Locate every Plasmodium ovale-infected red blood cell.
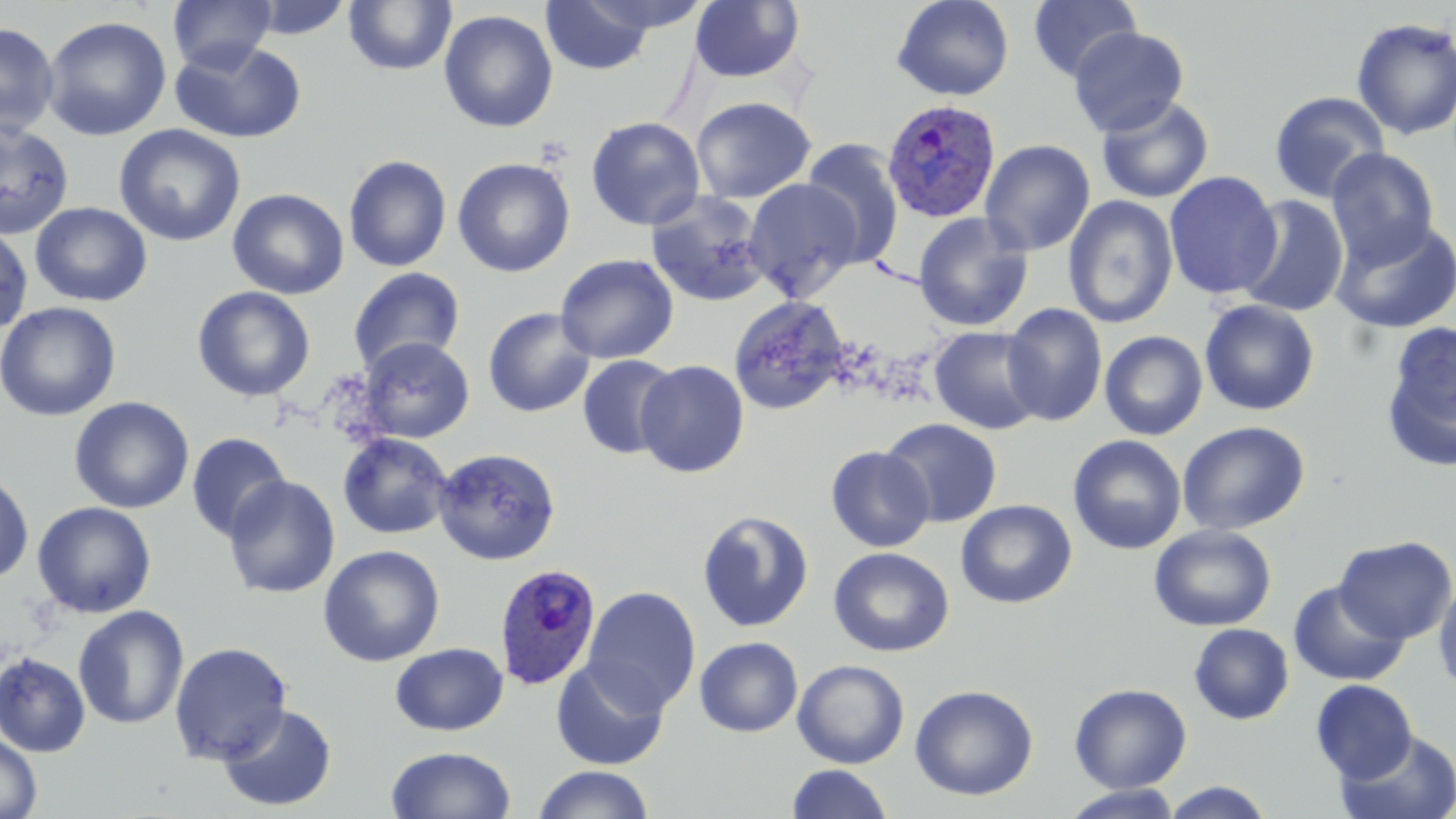

Approximate bounding boxes as (x1,y1)-(x2,y2) corner pairs in pixels.
Plasmodium ovale-infected red blood cells: (882,99)-(1001,223), (494,564)-(602,690).

{
  "slide_level_diagnosis": "Plasmodium ovale",
  "uninfected_red_blood_cell_locations": "approximate bounding boxes as (x1,y1)-(x2,y2) corner pairs in pixels: (168,0)-(276,73), (572,0)-(713,35), (891,0)-(1015,101), (1027,0)-(1142,83), (245,1)-(355,40), (343,1)-(457,75), (540,1)-(658,75), (690,1)-(805,83), (438,10)-(558,133), (42,15)-(172,141), (1350,17)-(1456,141), (0,23)-(59,137), (1069,26)-(1189,136), (170,38)-(306,145), (1269,91)-(1390,203), (690,96)-(816,203), (1095,96)-(1214,204), (586,116)-(705,230), (0,121)-(74,240), (114,124)-(246,247), (799,138)-(906,269), (979,139)-(1096,256), (1326,148)-(1439,266), (343,154)-(452,272), (452,157)-(575,278), (1164,171)-(1283,299), (743,178)-(864,301), (227,188)-(349,300), (646,190)-(769,307), (1236,195)-(1350,318), (1063,196)-(1178,328), (30,201)-(152,307), (913,212)-(1033,332), (1330,218)-(1456,335), (0,223)-(33,336), (555,253)-(679,364), (347,267)-(466,376), (192,286)-(315,401), (728,295)-(850,415), (1199,299)-(1320,416), (0,301)-(122,422), (1002,304)-(1107,426), (483,307)-(595,418), (1380,322)-(1456,471), (929,325)-(1047,435), (1099,331)-(1208,440), (358,337)-(474,442), (576,354)-(681,460), (636,359)-(750,478), (69,396)-(194,514), (881,418)-(1001,528), (1177,420)-(1310,536), (186,432)-(291,542), (337,433)-(453,540), (1067,434)-(1187,555), (825,445)-(935,552), (433,447)-(561,565), (0,469)-(34,584), (222,475)-(340,599), (956,500)-(1077,608), (32,502)-(156,618), (696,509)-(815,633), (1149,524)-(1277,631), (1335,535)-(1456,643), (318,544)-(445,667), (828,547)-(954,657), (1434,578)-(1456,693), (1288,580)-(1410,687), (582,586)-(701,715), (73,605)-(189,730), (1189,623)-(1294,725), (694,636)-(804,737), (168,641)-(293,764), (390,642)-(509,736), (0,652)-(91,757), (550,658)-(670,770), (792,660)-(909,768), (1310,679)-(1418,782), (1069,683)-(1192,793), (910,684)-(1039,801), (217,703)-(338,812), (1336,730)-(1456,819), (0,733)-(42,819), (385,745)-(516,819), (785,764)-(894,819), (532,765)-(655,819), (1159,782)-(1275,819), (1061,784)-(1186,818)",
  "stain": "May-Grünwald-Giemsa",
  "field_of_view": "one of a larger specimen",
  "image_size": "1456×819 pixels",
  "magnification": "1000x",
  "modality": "optical microscopy",
  "preparation": "thin blood film"
}